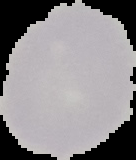
image size = 136×160 pixels
image type = cell region segmented out of the field of view; surrounding area masked to black
preparation = thin blood film
result = no Plasmodium parasites seen